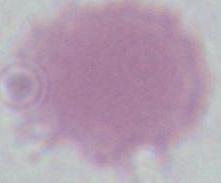

identification: erythrocyte
modality: micrograph
magnification: 1000x